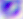
400x magnification. Photomicrograph. Toxoplasma gondii is shown.